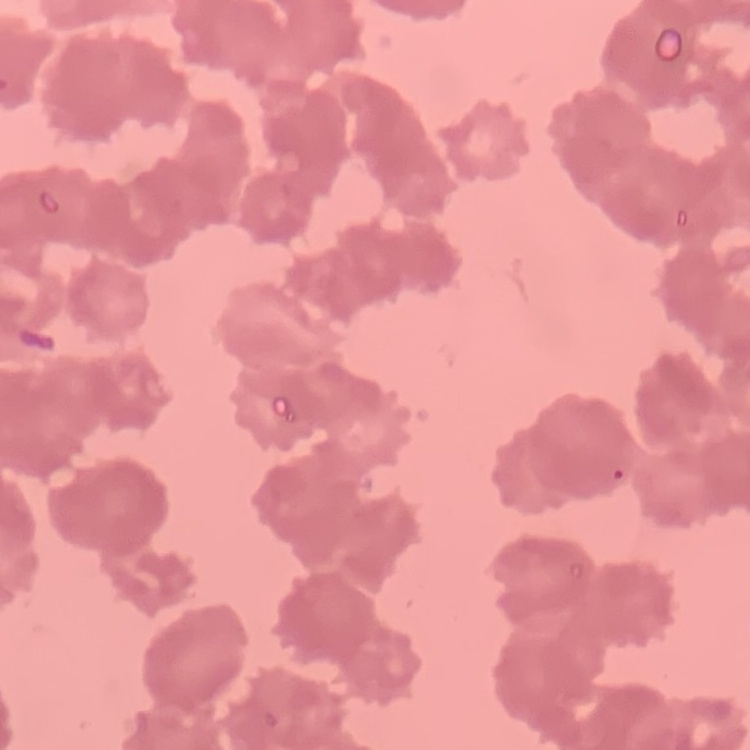

red blood cell morphology = rouleaux formation
image type = one tile cut from a larger photomicrograph
preparation = thin peripheral smear
stain = Field's or Giemsa